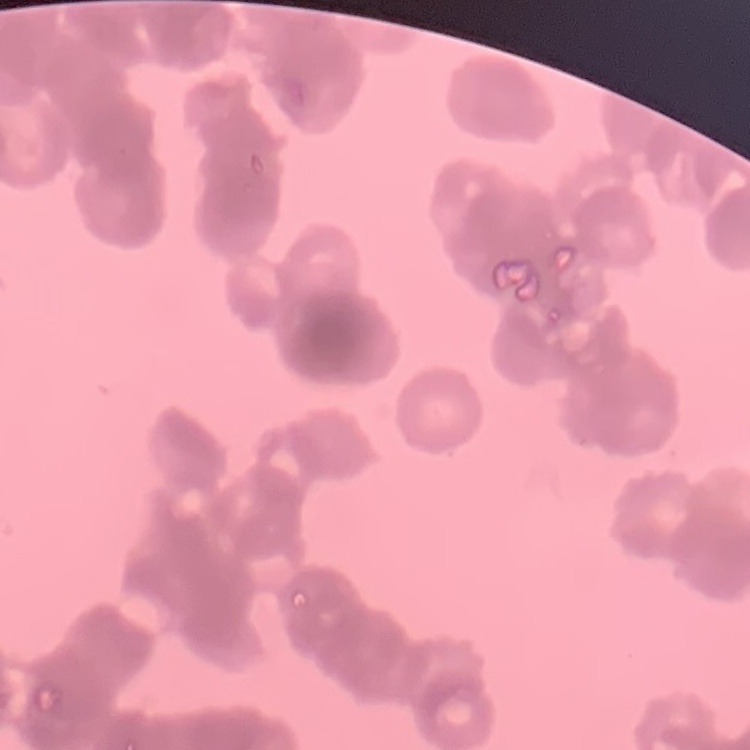
Summary:
  - Erythrocyte morphology: rouleaux formation
  - Stain: Field's or Giemsa
  - Image type: square crop of a larger photomicrograph
  - Preparation: thin blood smear